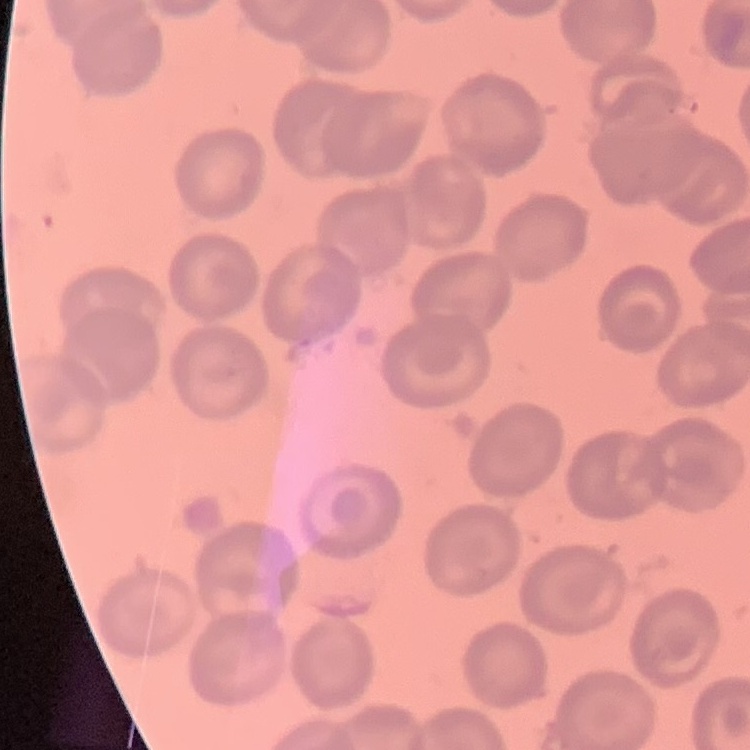 The erythrocytes show no rouleaux formation. One tile cut from a larger photomicrograph. Stained with either Field's or Giemsa. Thin blood smear.